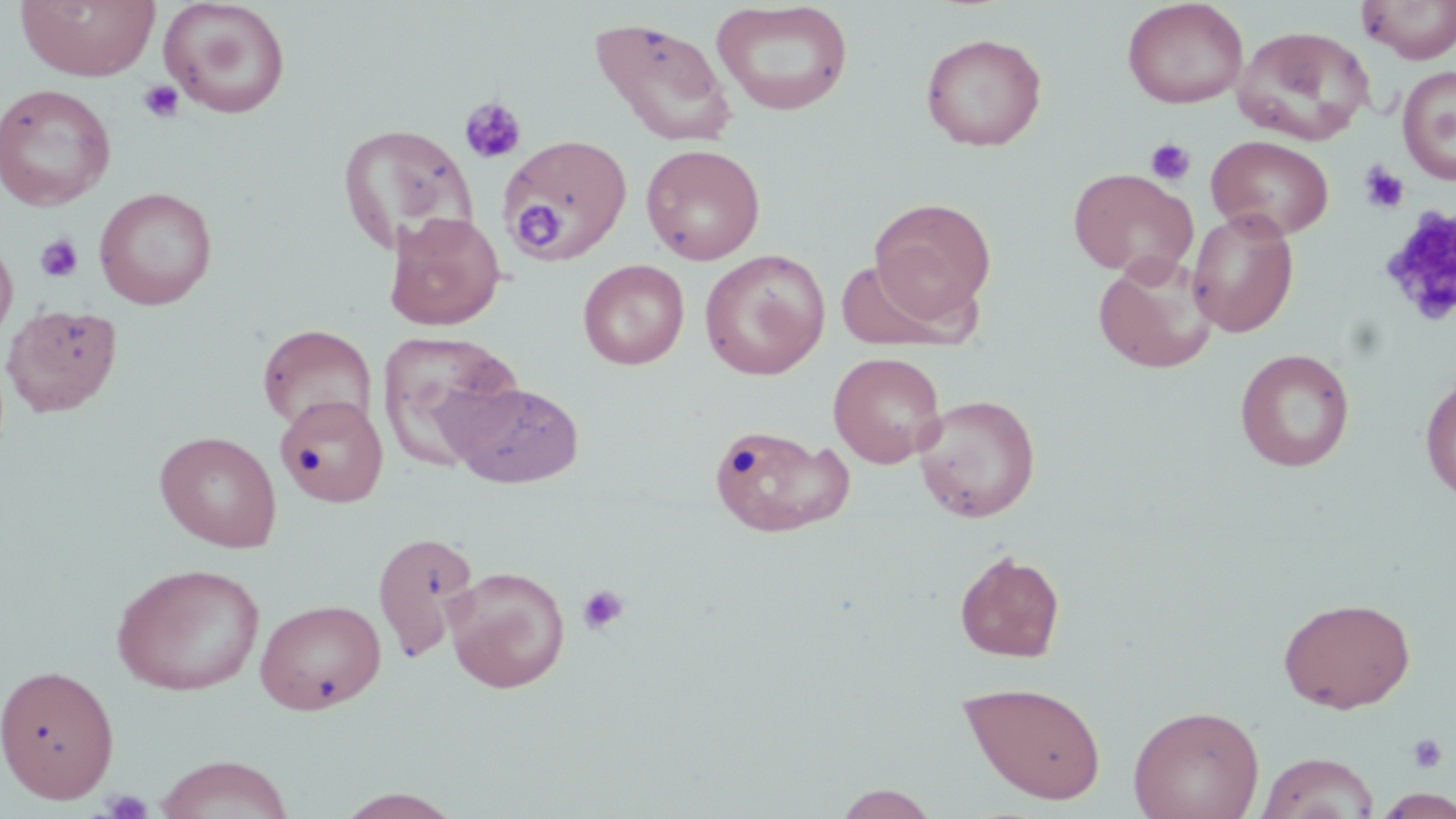

Approximate bounding boxes as (x1, y1, x2, y2) in pixels. Platelet locations: (138, 80, 184, 122), (459, 97, 527, 165), (1145, 137, 1196, 185), (1358, 161, 1410, 215), (516, 202, 562, 248), (1378, 207, 1456, 329), (35, 234, 83, 283), (576, 583, 630, 636), (1407, 733, 1449, 774), (101, 789, 154, 818). Uninfected red blood cell locations: (15, 0, 160, 82), (158, 0, 291, 119), (1122, 0, 1248, 109), (1358, 0, 1456, 63), (711, 2, 854, 116), (589, 17, 737, 147), (1233, 25, 1375, 145), (921, 32, 1047, 151), (1398, 65, 1456, 185), (0, 83, 116, 211), (339, 125, 478, 253), (499, 134, 631, 263), (1206, 135, 1334, 240), (641, 144, 765, 265), (1069, 168, 1197, 280), (94, 187, 218, 310), (869, 197, 996, 325), (1187, 209, 1299, 337), (384, 211, 505, 331), (0, 235, 18, 351), (699, 249, 830, 380), (1094, 253, 1216, 373), (578, 259, 689, 370), (837, 259, 956, 350), (2, 303, 122, 417), (258, 324, 377, 434), (377, 331, 524, 469), (1235, 348, 1356, 472), (829, 351, 946, 468), (1420, 374, 1456, 503), (444, 380, 585, 488), (278, 395, 388, 508), (913, 395, 1040, 522), (707, 423, 853, 539), (155, 431, 282, 553), (372, 531, 478, 661), (953, 550, 1066, 663), (111, 562, 265, 696), (443, 566, 570, 692), (1278, 596, 1416, 713), (255, 598, 386, 715), (0, 663, 120, 803), (958, 680, 1107, 804), (1128, 704, 1265, 819), (1255, 751, 1379, 819), (154, 755, 295, 819), (829, 783, 941, 818), (1375, 788, 1456, 818), (333, 789, 464, 819). Slide-level diagnosis: no evidence of blood parasites. Light microscopy. May-Grünwald-Giemsa-stained preparation. Image is 1456×819 pixels. Thin blood film. Captured at 1000x magnification. One field of a larger specimen.